Classify this cell by malaria status.
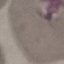

It is uninfected.

{
  "stain": "Giemsa",
  "image_type": "automatically extracted cell patch, resized to 64 × 64 pixels",
  "preparation": "thin blood film",
  "capture": "smartphone through the microscope eyepiece"
}